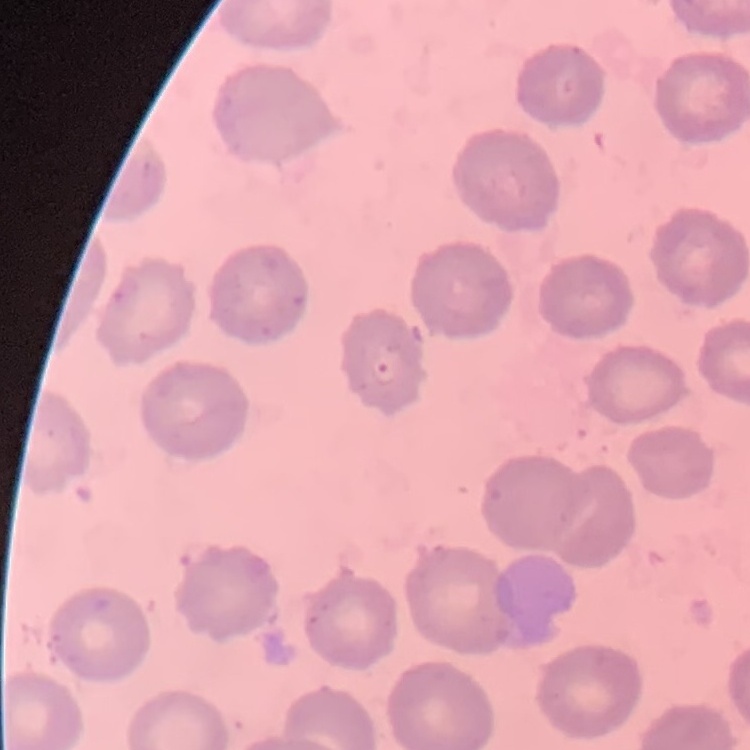
Summary:
  - Erythrocyte morphology: no rouleaux formation
  - Stain: Field's or Giemsa
  - Image type: square crop of a larger photomicrograph
  - Preparation: thin peripheral smear